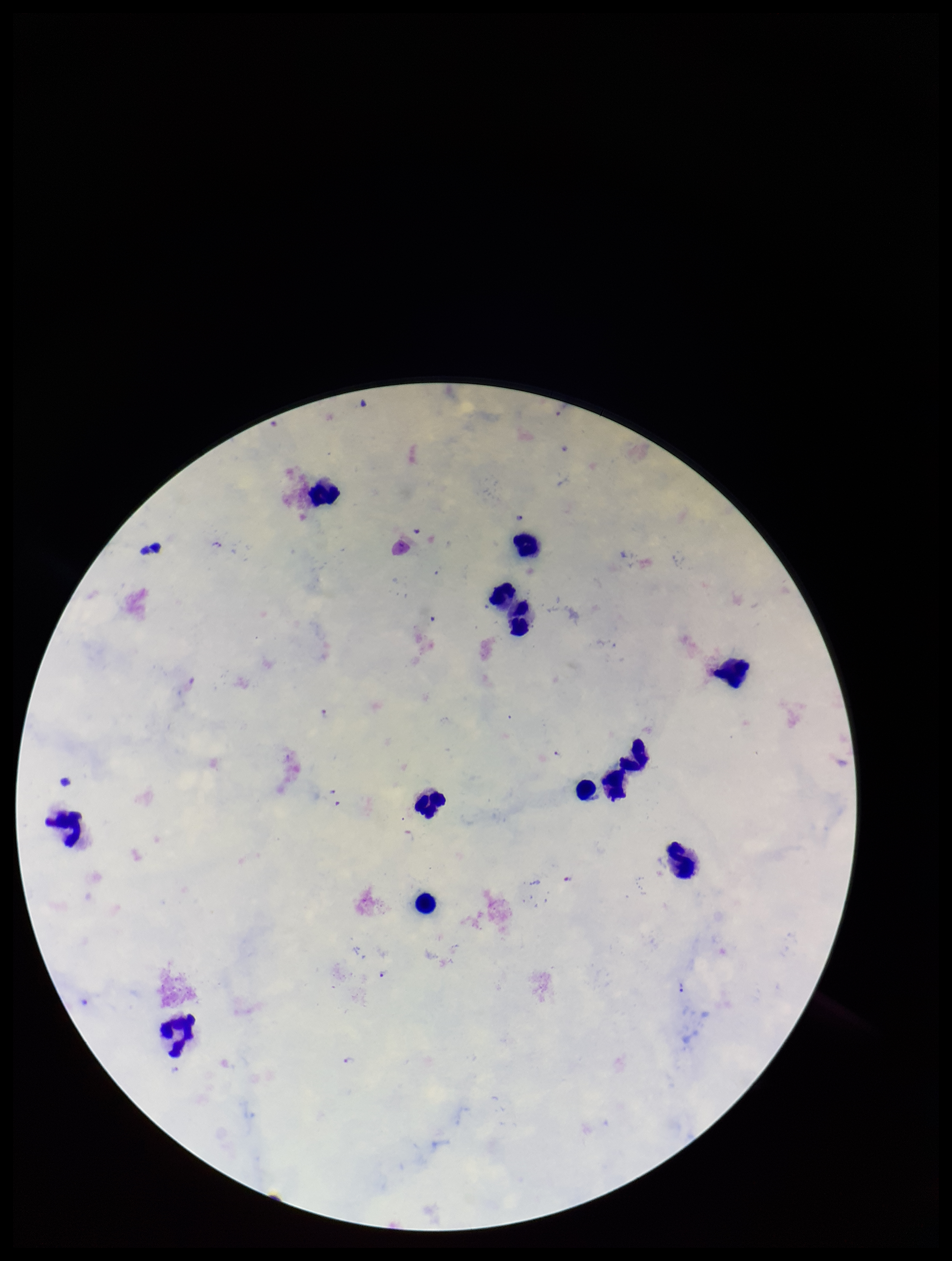

Summary:
  - Preparation: thick
  - Parasite count: 2
  - Plasmodium parasites: identified
  - Species reported for this patient: Plasmodium falciparum
  - Field of view: single
  - Image size: 952×1261 pixels
  - Stain: Giemsa
  - Patient malaria status: positive
  - Capture: smartphone photograph through the microscope eyepiece
  - Leukocyte count: 13